Report the malaria status of this cell.
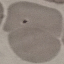
It is uninfected.

Summary:
  - Stain: Giemsa
  - Image type: cell patch, automatically extracted from a larger field of view and resized to 64 × 64 pixels
  - Capture: smartphone camera at the microscope eyepiece
  - Preparation: thin blood film